Report the malaria status of this cell.
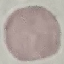

Uninfected.

{
  "preparation": "thin blood film",
  "capture": "smartphone through the microscope eyepiece",
  "stain": "Giemsa",
  "image_type": "cell patch, automatically extracted from a larger field of view and resized to 64 × 64 pixels"
}